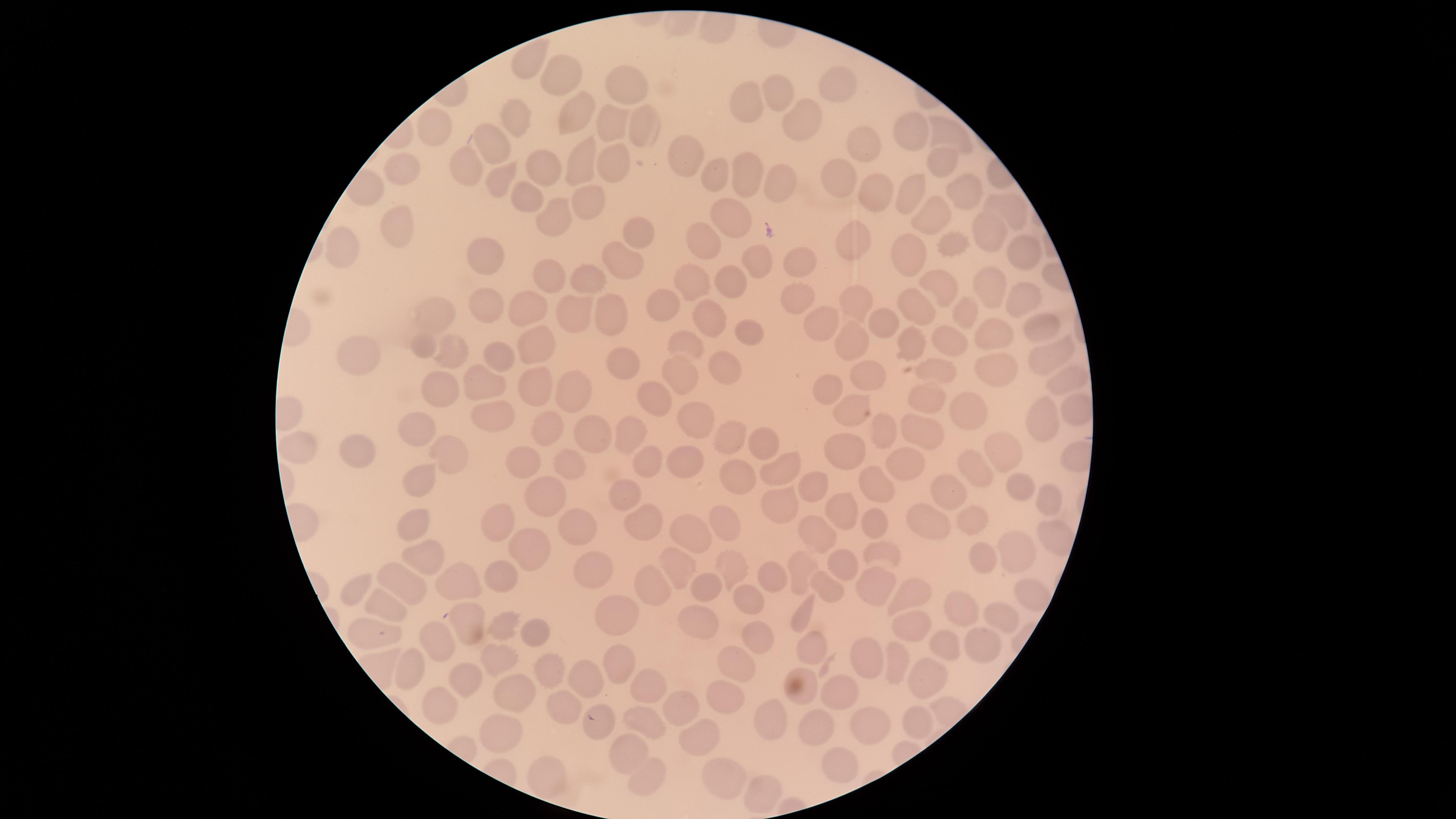
Approximate marker points, in pixels from the top-left corner. Uninfected RBCs: (x=560, y=69), (x=839, y=85), (x=626, y=86), (x=782, y=90), (x=754, y=105), (x=577, y=113), (x=808, y=120), (x=515, y=121), (x=611, y=122), (x=643, y=128), (x=915, y=128), (x=429, y=130), (x=949, y=133), (x=489, y=146), (x=869, y=147), (x=616, y=157), (x=684, y=158), (x=941, y=161), (x=585, y=164), (x=472, y=169), (x=542, y=170), (x=841, y=176), (x=741, y=177), (x=400, y=178), (x=496, y=179), (x=716, y=179), (x=782, y=180), (x=875, y=190), (x=906, y=191), (x=964, y=193), (x=524, y=197), (x=587, y=204), (x=1012, y=213), (x=938, y=214), (x=558, y=218), (x=732, y=221), (x=993, y=229), (x=393, y=234), (x=639, y=235), (x=708, y=236), (x=859, y=238), (x=956, y=242), (x=348, y=249), (x=911, y=251), (x=1027, y=253), (x=484, y=255), (x=758, y=256), (x=805, y=264), (x=628, y=270), (x=546, y=274), (x=588, y=277), (x=734, y=281), (x=993, y=285), (x=940, y=286), (x=699, y=288), (x=1023, y=295), (x=804, y=298), (x=858, y=299), (x=487, y=303), (x=535, y=303), (x=676, y=307), (x=922, y=310), (x=967, y=312), (x=438, y=314), (x=573, y=314), (x=609, y=317), (x=884, y=318), (x=824, y=319), (x=714, y=320), (x=1036, y=325), (x=747, y=333), (x=849, y=335), (x=993, y=338), (x=945, y=339), (x=911, y=341), (x=535, y=344), (x=687, y=346), (x=423, y=348), (x=458, y=351), (x=495, y=354), (x=618, y=356), (x=1050, y=356), (x=369, y=359), (x=727, y=367), (x=872, y=371), (x=1001, y=372), (x=943, y=374), (x=686, y=378), (x=1067, y=379), (x=534, y=386), (x=582, y=388), (x=490, y=389), (x=443, y=392), (x=832, y=393), (x=663, y=399), (x=934, y=403), (x=854, y=404), (x=1043, y=411), (x=972, y=412), (x=493, y=413), (x=704, y=415), (x=415, y=429), (x=885, y=429), (x=927, y=431), (x=544, y=432), (x=629, y=434), (x=595, y=435), (x=733, y=436), (x=760, y=446), (x=298, y=447), (x=1006, y=447), (x=351, y=450), (x=453, y=454), (x=855, y=454), (x=527, y=460), (x=564, y=460), (x=651, y=463), (x=686, y=464), (x=905, y=464), (x=776, y=468), (x=976, y=468), (x=741, y=475), (x=428, y=480), (x=1019, y=483), (x=811, y=485), (x=949, y=489), (x=871, y=490), (x=626, y=497), (x=548, y=499), (x=1044, y=499), (x=779, y=504), (x=844, y=512), (x=971, y=517), (x=415, y=520), (x=934, y=521), (x=645, y=523), (x=723, y=523), (x=873, y=525), (x=500, y=526), (x=577, y=528), (x=813, y=534), (x=695, y=537), (x=1017, y=548), (x=531, y=551), (x=882, y=554), (x=425, y=555), (x=982, y=557), (x=840, y=562), (x=731, y=567), (x=595, y=569), (x=679, y=570), (x=802, y=570), (x=774, y=576), (x=498, y=578), (x=703, y=581), (x=404, y=582), (x=462, y=582), (x=875, y=586), (x=827, y=588), (x=653, y=589), (x=358, y=591), (x=1028, y=591), (x=905, y=597), (x=749, y=599), (x=385, y=602), (x=959, y=610), (x=803, y=611), (x=617, y=615), (x=1000, y=618), (x=463, y=620), (x=697, y=622), (x=908, y=624), (x=503, y=628), (x=754, y=631), (x=375, y=634), (x=538, y=634), (x=432, y=642), (x=946, y=644), (x=808, y=647), (x=976, y=647), (x=870, y=653), (x=498, y=657), (x=892, y=660), (x=408, y=668), (x=546, y=668), (x=618, y=668), (x=738, y=668), (x=922, y=674), (x=468, y=676), (x=583, y=684), (x=806, y=684), (x=644, y=688), (x=839, y=689), (x=510, y=690), (x=727, y=698), (x=440, y=702), (x=676, y=707), (x=562, y=709), (x=913, y=721), (x=779, y=722), (x=641, y=723), (x=818, y=727), (x=868, y=727), (x=696, y=735), (x=497, y=737), (x=625, y=757), (x=842, y=764), (x=734, y=771), (x=551, y=778), (x=650, y=782), (x=758, y=795). Image is 1456×819 pixels. Giemsa-stained preparation. Thin smear of blood. Single field of view. Smartphone photograph through the microscope eyepiece. Circular visible region. Presence: no malaria parasites identified.